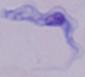 A trypanosome is seen. Captured at 1000x magnification. Micrograph.